State which parasite is depicted.
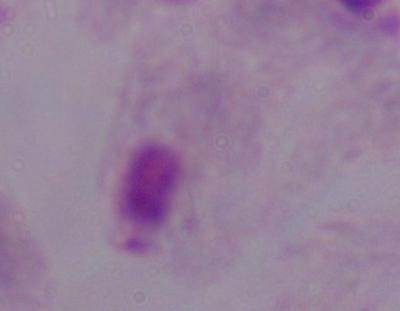

A trichomonad.

1000x magnification. Micrograph.